Locate every blood parasite and identify its species.
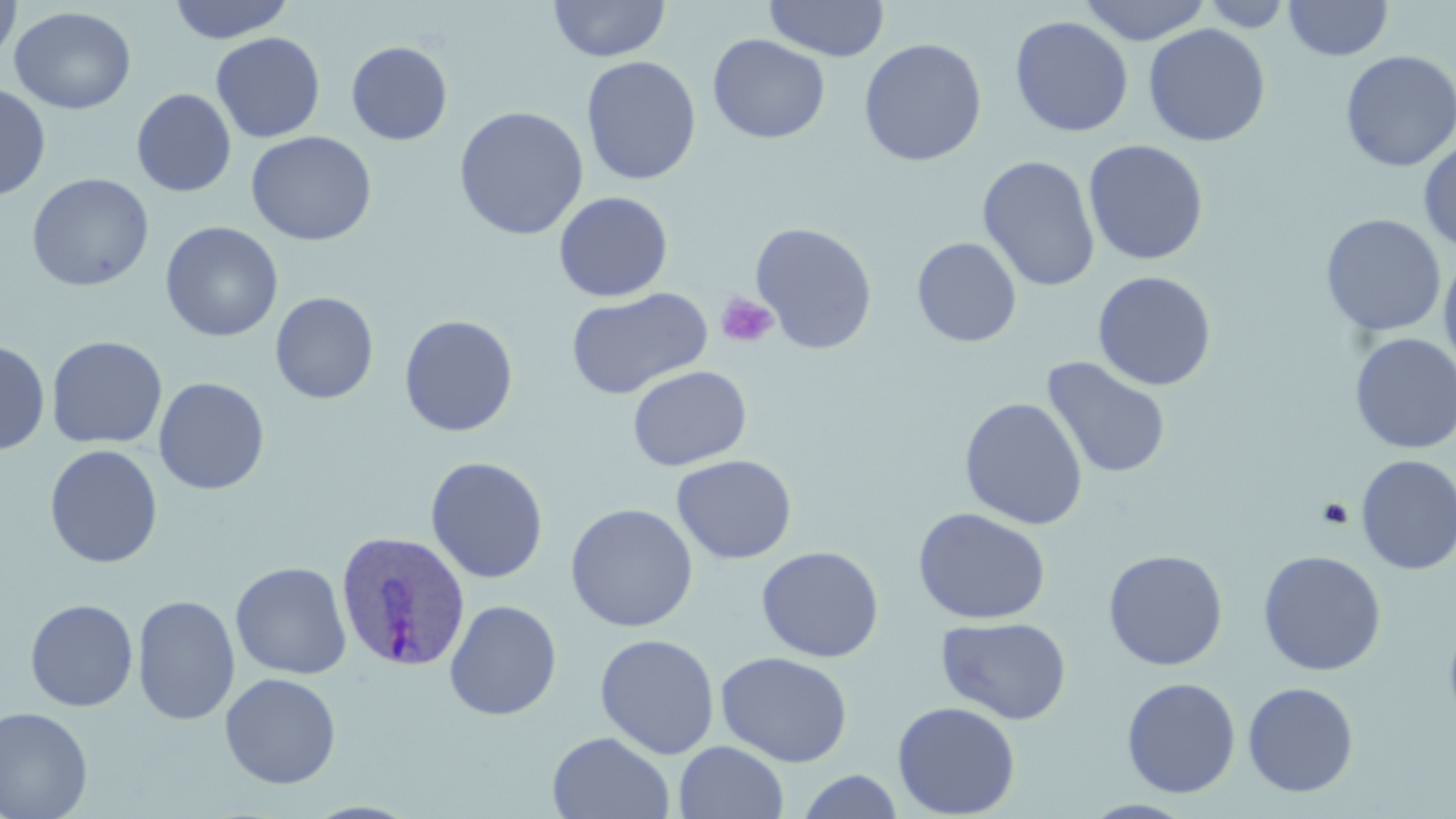

Approximate bounding boxes as (x1,y1)-(x2,y2) corner pairs in pixels.
Plasmodium ovale-infected red blood cells: (335,531)-(472,672).
No Plasmodium falciparum, Plasmodium malariae, Plasmodium vivax, Babesia divergens, or Trypanosoma brucei observed.

slide-level diagnosis = Plasmodium ovale
image size = 1456×819 pixels
field of view = single
modality = light microscopy
magnification = 1000x
preparation = thin blood film
stain = May-Grünwald-Giemsa
platelet locations = approximate bounding boxes as (x1,y1)-(x2,y2) corner pairs in pixels: (715,291)-(779,348), (1317,498)-(1354,529)
uninfected red blood cell locations = approximate bounding boxes as (x1,y1)-(x2,y2) corner pairs in pixels: (0,0)-(22,68), (167,0)-(294,43), (548,0)-(671,62), (763,0)-(890,62), (1078,0)-(1212,45), (1197,1)-(1296,31), (1284,1)-(1393,61), (9,6)-(136,114), (1009,15)-(1134,137), (1143,23)-(1271,147), (210,32)-(326,143), (707,34)-(831,144), (858,37)-(987,166), (346,41)-(453,145), (1340,50)-(1456,172), (581,55)-(701,186), (0,83)-(51,200), (131,88)-(236,197), (453,105)-(589,240), (245,131)-(377,246), (1418,138)-(1456,253), (1084,139)-(1208,265), (977,155)-(1101,293), (26,172)-(154,292), (553,191)-(674,302), (1321,214)-(1446,336), (160,221)-(283,342), (750,222)-(879,354), (911,236)-(1022,348), (1438,251)-(1456,380), (1092,270)-(1217,391), (565,287)-(713,400), (270,292)-(379,404), (399,314)-(519,438), (1350,333)-(1456,454), (47,335)-(168,449), (0,339)-(50,455), (1041,357)-(1172,480), (627,365)-(752,471), (153,377)-(270,495), (959,396)-(1088,530), (44,444)-(163,568), (671,454)-(797,564), (1355,454)-(1456,575), (425,456)-(549,584), (565,502)-(699,632), (913,507)-(1051,625), (756,545)-(884,663), (1103,549)-(1228,671), (1258,549)-(1387,676), (230,561)-(352,680), (132,594)-(240,726), (24,598)-(138,711), (444,599)-(562,720), (1443,609)-(1456,735), (936,616)-(1072,725), (595,633)-(721,759), (715,651)-(853,767), (220,673)-(341,789), (1121,677)-(1241,798), (1242,681)-(1359,797), (892,700)-(1021,818), (0,706)-(94,819), (547,731)-(675,818), (673,741)-(789,819), (795,769)-(905,819)